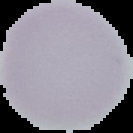
The area outside the segmented cell region is set to black. Image is 133×133 pixels. From a thin blood smear. Result: no Plasmodium parasites seen.